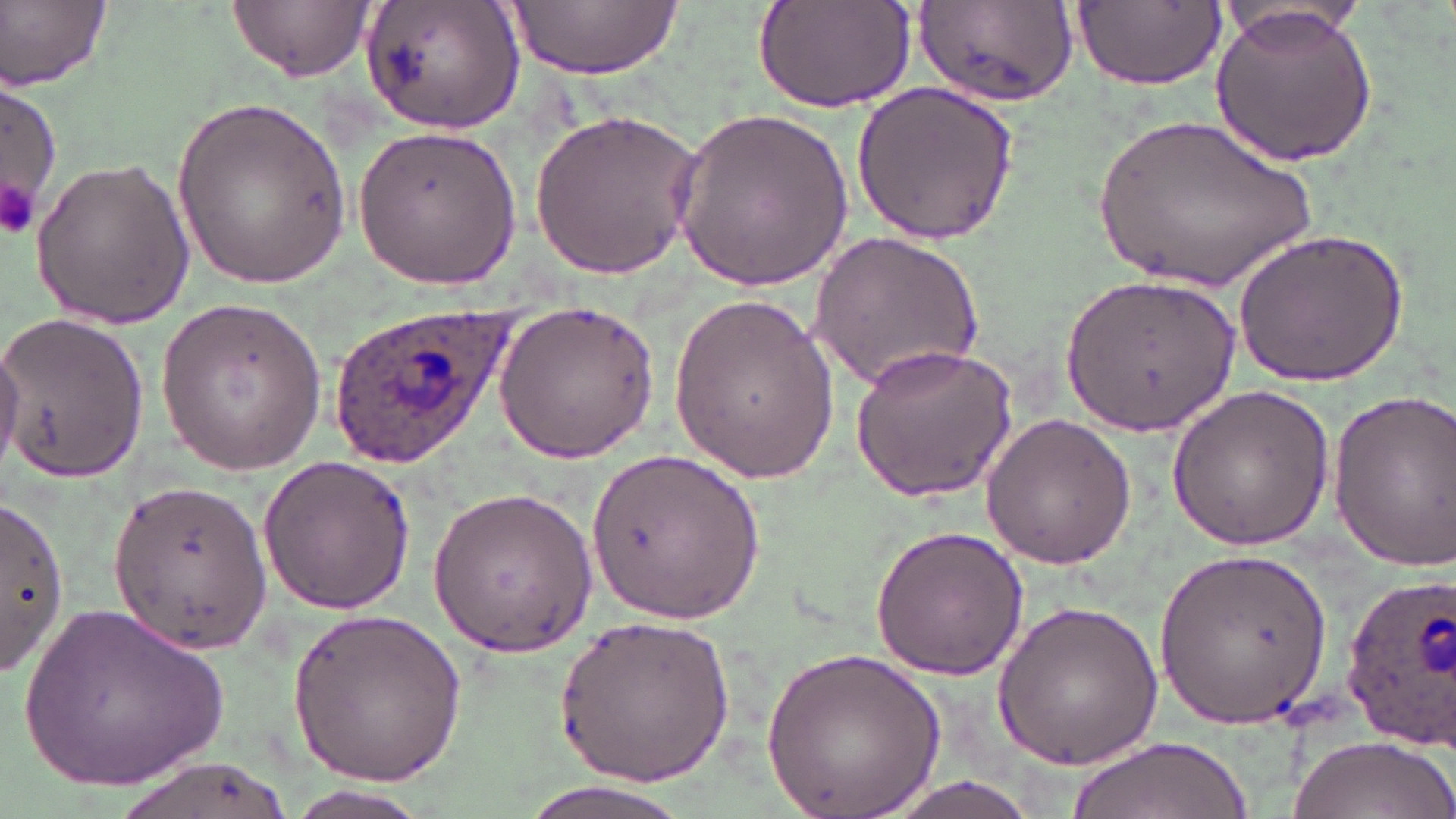
slide-level diagnosis = Plasmodium ovale
uninfected red blood cell locations = approximate bounding boxes as (x1, y1, x2, y2) in pixels: (2, 0, 111, 90), (228, 0, 371, 81), (361, 0, 527, 138), (504, 0, 681, 82), (754, 1, 916, 115), (1075, 1, 1226, 88), (1216, 1, 1373, 51), (912, 3, 1078, 108), (1211, 4, 1377, 170), (0, 77, 61, 229), (852, 81, 1023, 245), (173, 92, 351, 290), (671, 104, 855, 292), (527, 105, 707, 282), (1086, 108, 1326, 302), (354, 124, 519, 290), (28, 154, 194, 329), (1234, 225, 1408, 386), (810, 230, 984, 393), (1063, 274, 1241, 435), (668, 290, 838, 483), (155, 296, 326, 473), (492, 299, 664, 464), (0, 313, 150, 484), (0, 332, 26, 471), (849, 341, 1019, 502), (1164, 384, 1335, 553), (1323, 386, 1456, 568), (980, 413, 1138, 569), (584, 444, 771, 630), (258, 454, 415, 614), (109, 476, 273, 656), (427, 485, 597, 658), (0, 492, 67, 676), (870, 523, 1029, 681), (1154, 545, 1331, 729), (18, 596, 233, 792), (994, 598, 1164, 772), (289, 606, 466, 783), (555, 610, 734, 785), (761, 644, 946, 819), (1288, 732, 1453, 819), (1066, 736, 1252, 819), (106, 752, 300, 819), (860, 774, 1063, 819), (505, 778, 697, 819), (280, 788, 438, 819)
modality = optical microscopy
Plasmodium ovale-infected red blood cell locations = approximate bounding boxes as (x1, y1, x2, y2) in pixels: (323, 303, 521, 467), (1339, 569, 1455, 751)
magnification = 1000x
stain = May-Grünwald-Giemsa
image size = 1456×819 pixels
preparation = thin blood film
platelet locations = approximate bounding boxes as (x1, y1, x2, y2) in pixels: (0, 174, 43, 241)
field of view = one of a larger specimen